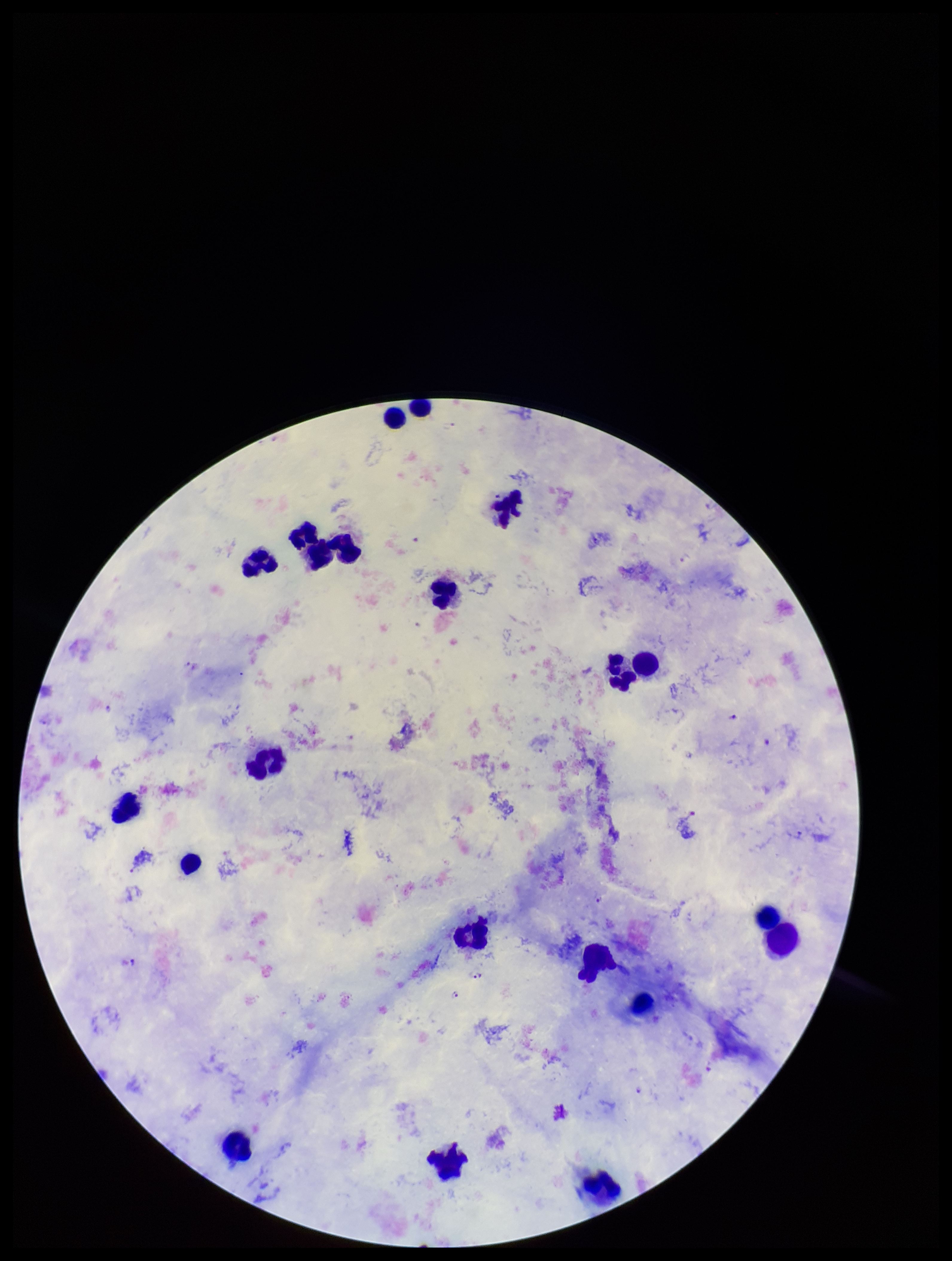

Plasmodium parasites = detected
preparation = thick
patient malaria status = infected
species reported for this patient = Plasmodium falciparum
leukocyte count = 21
image size = 952×1261 pixels
stain = Giemsa
parasite count = 10
capture = smartphone photograph through the microscope eyepiece
field of view = one from this slide